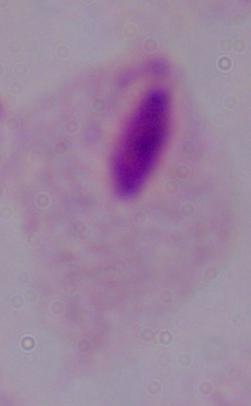

Summary:
  - Identification: trichomonad
  - Modality: micrograph
  - Magnification: 1000x